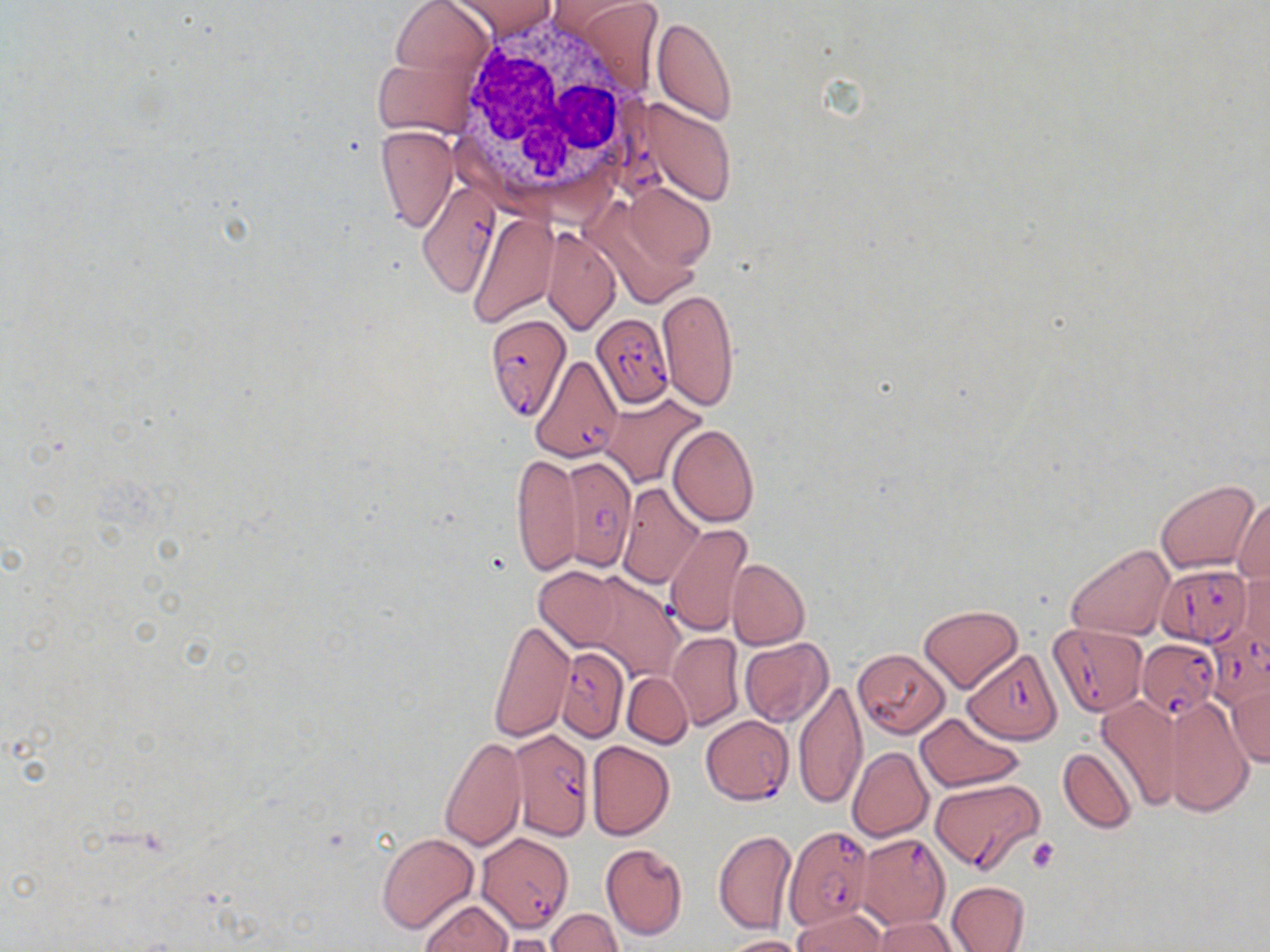
Summary:
  - Coordinate format: approximate bounding boxes as (x1,y1)-(x2,y2) corner pairs in pixels
  - White blood cell locations: (452,13)-(656,206)
  - Platelet locations: (1026,837)-(1061,872)
  - Uninfected red blood cell locations: (382,0)-(496,88), (449,0)-(557,40), (552,0)-(664,92), (652,17)-(738,125), (373,41)-(485,139), (645,99)-(737,206), (375,125)-(457,232), (622,183)-(714,271), (467,213)-(559,325), (542,227)-(619,334), (658,290)-(738,409), (600,394)-(708,487), (667,425)-(759,527), (511,452)-(580,575), (1154,478)-(1260,574), (616,483)-(704,588), (1234,497)-(1270,587), (662,523)-(753,635), (1066,544)-(1175,641), (726,558)-(809,651), (535,568)-(620,649), (1238,568)-(1269,653), (579,572)-(684,684), (919,605)-(1022,692), (489,618)-(573,743), (668,633)-(742,730), (739,638)-(833,728), (853,648)-(953,743), (621,672)-(693,747), (795,680)-(867,809), (1227,680)-(1269,768), (1165,695)-(1253,817), (1098,696)-(1183,810), (916,712)-(1024,792), (439,735)-(526,852), (587,741)-(673,840), (847,747)-(934,842), (1057,747)-(1137,834), (713,828)-(795,934), (375,833)-(478,935), (600,843)-(688,940), (947,881)-(1029,951), (420,899)-(513,952), (793,907)-(888,951), (546,909)-(623,952), (871,917)-(960,952), (495,935)-(566,952), (719,935)-(811,952)
  - Plasmodium falciparum-infected red blood cell locations: (416,177)-(501,295), (590,313)-(673,408), (484,315)-(569,420), (534,335)-(635,451), (561,456)-(636,568), (1155,565)-(1251,647), (1048,623)-(1148,715), (1205,626)-(1270,710), (1137,638)-(1219,718), (554,646)-(629,742), (964,648)-(1064,744), (701,716)-(794,803), (509,728)-(596,839), (931,778)-(1043,873), (784,826)-(876,930), (477,833)-(574,933), (855,833)-(950,929)
  - Slide-level diagnosis: Plasmodium falciparum
  - Preparation: thin blood smear
  - Field of view: one of a larger specimen
  - Magnification: 1000x
  - Modality: light microscopy
  - Image size: 1270×952 pixels
  - Stain: May-Grünwald-Giemsa